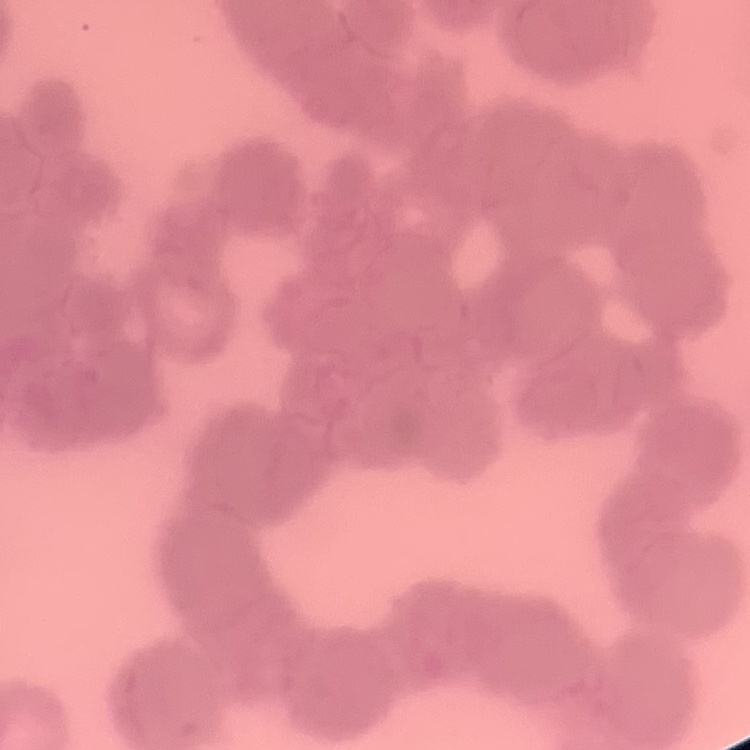

red blood cell morphology = rouleaux formation
stain = Field's or Giemsa
preparation = thin peripheral smear
image type = one tile cut from a larger photomicrograph